Report the malaria status.
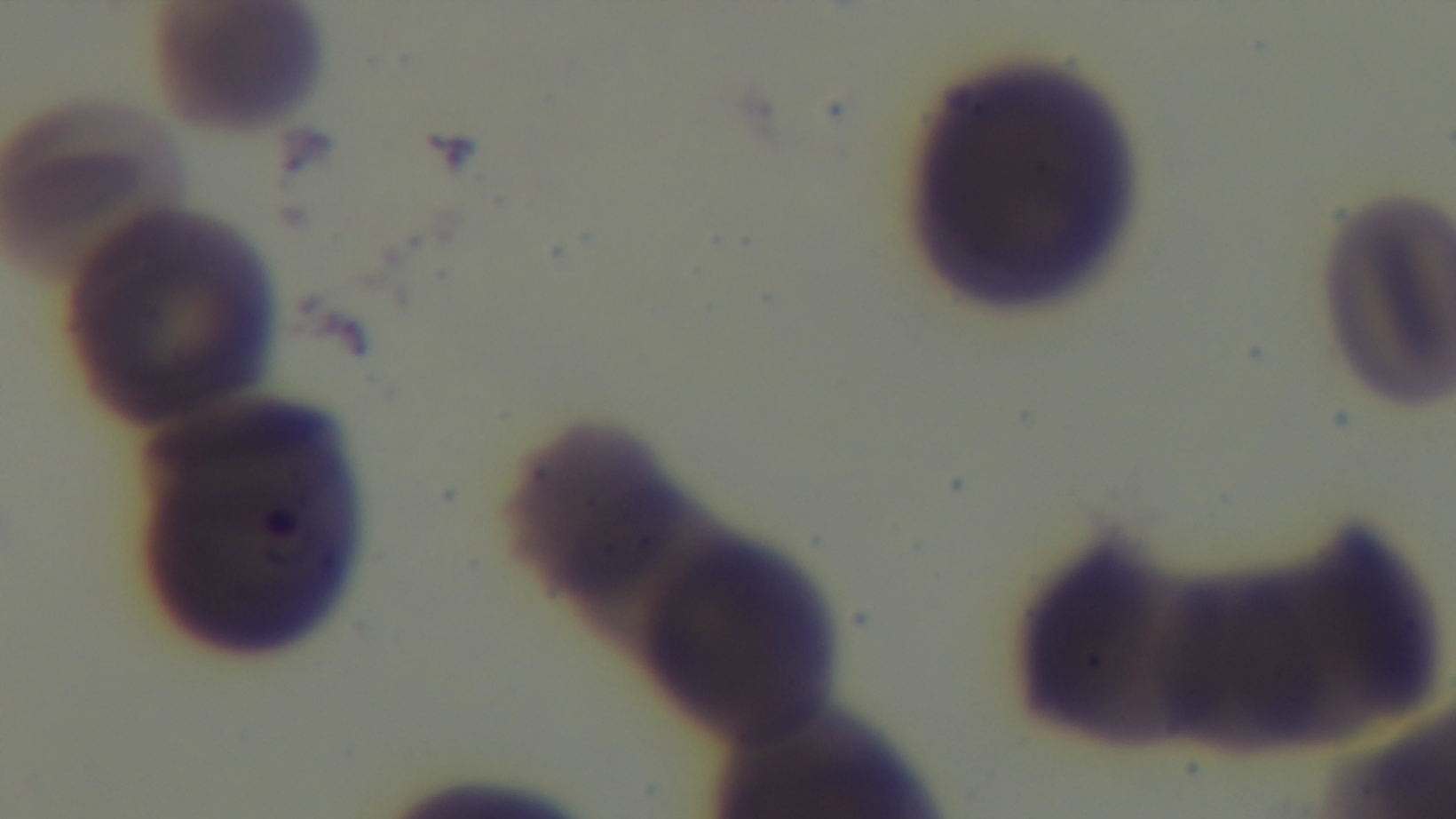

Positive.

Summary:
  - Objective: 100x oil immersion
  - Stain: Giemsa
  - Preparation: thin smear
  - Capture: mounted 4K digital camera
  - Modality: light microscopy
  - Field of view: single